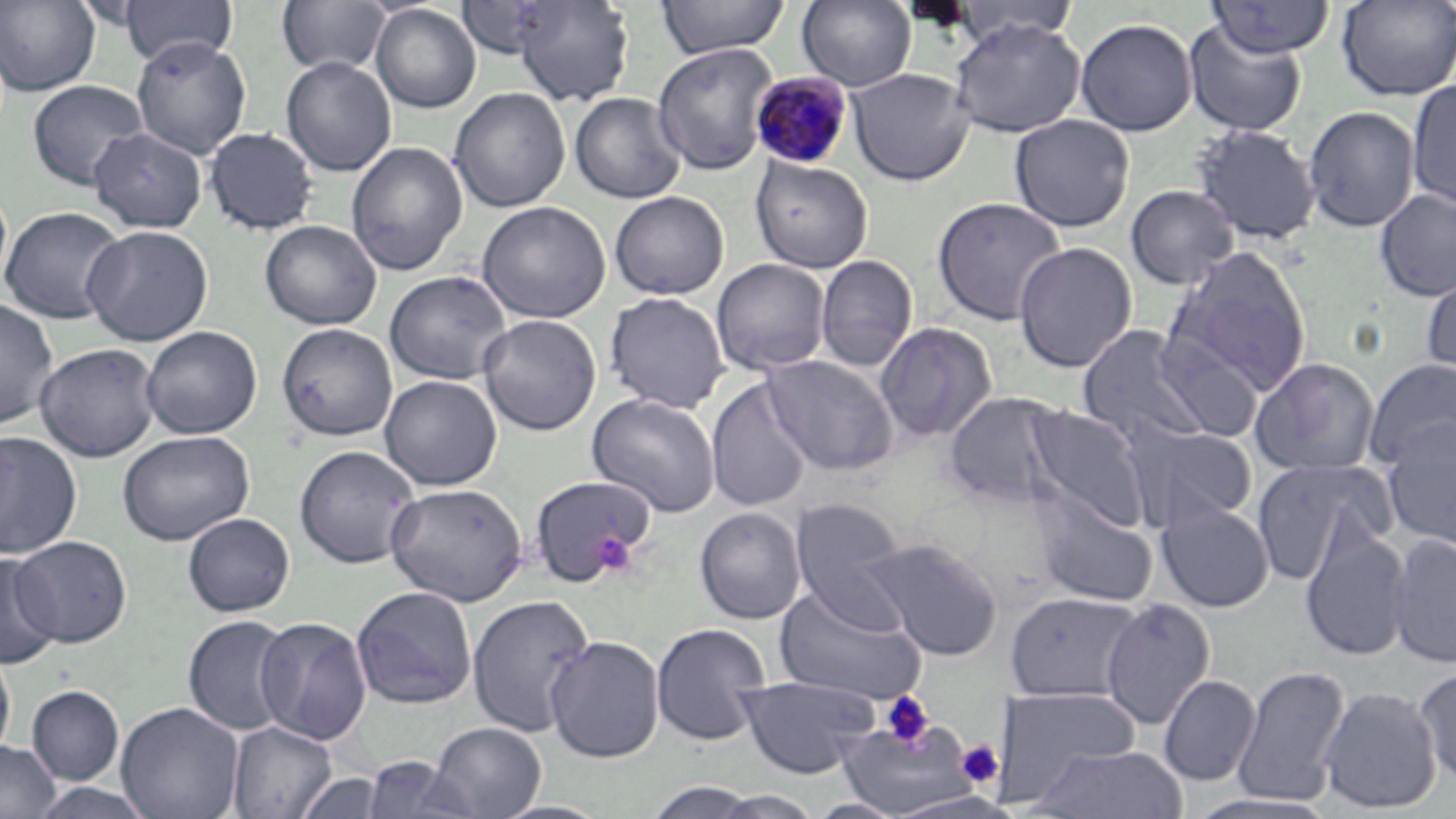
Summary:
  - Coordinate format: approximate bounding boxes as (x1,y1)-(x2,y2) corner pairs in pixels
  - Uninfected red blood cell locations: (510,0)-(635,106), (655,0)-(790,59), (796,0)-(918,91), (951,0)-(1079,47), (1337,0)-(1456,100), (0,1)-(100,95), (119,1)-(237,68), (276,1)-(392,75), (458,1)-(561,59), (1202,1)-(1336,58), (370,3)-(482,112), (1075,18)-(1198,136), (949,19)-(1085,138), (1183,19)-(1308,136), (131,37)-(252,159), (652,43)-(778,176), (281,56)-(397,176), (848,68)-(974,185), (1406,78)-(1456,210), (27,79)-(149,191), (449,87)-(570,212), (570,92)-(686,203), (1302,105)-(1420,232), (1009,114)-(1135,232), (1191,124)-(1321,244), (89,127)-(208,232), (204,127)-(319,235), (346,142)-(468,276), (750,155)-(873,272), (0,183)-(12,295), (1125,184)-(1240,290), (1374,188)-(1456,301), (610,191)-(729,299), (932,197)-(1067,326), (477,201)-(611,322), (1142,202)-(1283,334), (0,206)-(128,324), (260,220)-(382,329), (82,225)-(213,345), (1013,241)-(1137,373), (1168,248)-(1312,393), (816,255)-(918,371), (712,258)-(831,375), (1420,265)-(1456,387), (384,270)-(512,384), (605,291)-(730,412), (0,297)-(59,429), (478,314)-(601,435), (875,321)-(998,444), (277,323)-(398,441), (288,324)-(406,567), (1077,324)-(1215,449), (141,326)-(262,439), (1152,332)-(1265,442), (35,343)-(161,461), (763,354)-(899,475), (1250,357)-(1380,476), (1363,358)-(1456,472), (380,374)-(503,490), (706,378)-(814,512), (943,391)-(1072,510), (586,392)-(722,517), (1022,405)-(1151,533), (1380,418)-(1456,552), (1123,422)-(1257,531), (0,430)-(82,559), (117,430)-(254,545), (294,444)-(422,568), (1251,459)-(1392,585), (527,473)-(657,587), (385,482)-(528,605), (1034,496)-(1158,607), (790,497)-(909,620), (1155,500)-(1275,613), (695,506)-(807,624), (183,513)-(295,616), (1299,520)-(1411,661), (1387,533)-(1456,669), (9,536)-(132,646), (864,537)-(1004,660), (0,553)-(62,669), (774,585)-(926,706), (352,586)-(477,709), (1005,591)-(1143,703), (467,594)-(596,737), (1100,598)-(1216,729), (183,615)-(296,736), (255,616)-(373,745), (651,623)-(772,746), (545,635)-(665,763), (0,648)-(15,762), (1232,664)-(1350,806), (1414,665)-(1455,787), (1159,674)-(1260,786), (737,675)-(880,778), (26,685)-(124,785), (1318,685)-(1442,814), (995,687)-(1142,802), (116,702)-(245,819), (836,715)-(979,817), (228,721)-(337,818), (428,721)-(546,819), (0,739)-(61,819), (1027,743)-(1187,818), (361,757)-(476,818), (292,772)-(390,818), (29,782)-(156,819), (642,782)-(768,817), (708,790)-(826,819), (882,792)-(1025,818), (1184,792)-(1342,817), (808,797)-(906,818), (489,800)-(615,819)
  - Platelet locations: (591,530)-(636,576), (879,691)-(936,751), (956,738)-(1004,789)
  - Plasmodium malariae-infected red blood cell locations: (750,73)-(853,169)
  - Slide-level diagnosis: Plasmodium malariae
  - Preparation: thin blood smear
  - Stain: May-Grünwald-Giemsa
  - Modality: optical microscopy
  - Field of view: single
  - Image size: 1456×819 pixels
  - Magnification: 1000x